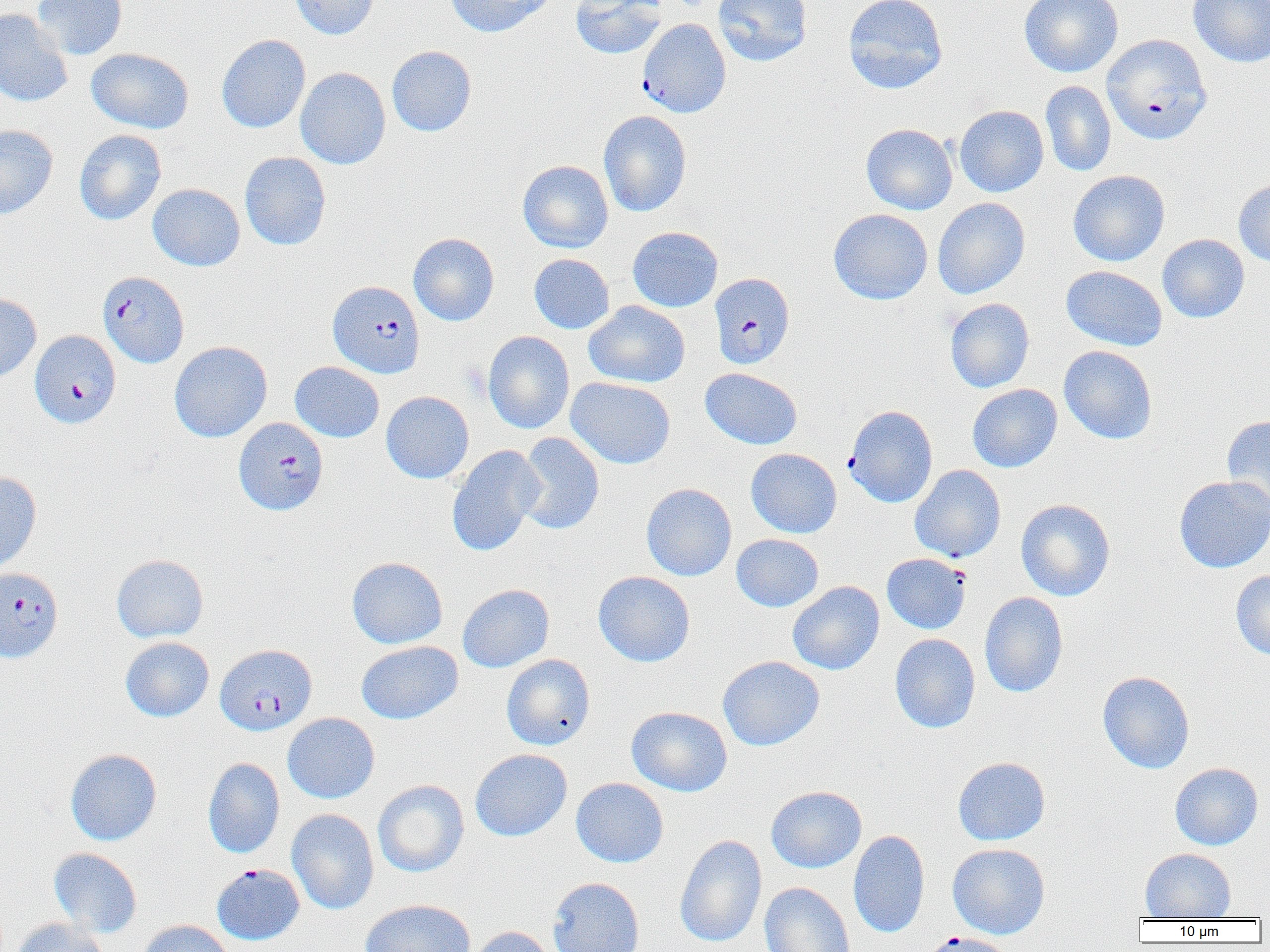
slide-level diagnosis = Plasmodium falciparum
field of view = one of a larger specimen
magnification = 1000x
uninfected red blood cell locations (subset) = approximate bounding boxes as [x1, y1, x2, y2] in pixels: [32, 0, 127, 60], [289, 0, 378, 40], [445, 0, 556, 37], [570, 0, 668, 60], [713, 0, 813, 66], [843, 0, 948, 94], [1019, 0, 1123, 78], [1187, 0, 1270, 68], [0, 9, 73, 107], [216, 34, 310, 133], [387, 45, 477, 136], [86, 48, 194, 133], [295, 67, 391, 170], [1040, 80, 1116, 177], [954, 105, 1048, 198], [598, 110, 692, 217], [860, 123, 958, 215], [0, 124, 58, 220], [74, 130, 166, 226], [239, 152, 331, 251], [517, 160, 613, 253], [1068, 170, 1170, 267], [1233, 179, 1270, 267], [148, 183, 245, 271], [932, 197, 1030, 299], [828, 208, 933, 304], [627, 226, 723, 312], [408, 233, 499, 326], [1157, 234, 1249, 323], [529, 253, 614, 334], [1060, 265, 1167, 351], [0, 293, 42, 384], [945, 298, 1034, 393], [584, 301, 689, 388], [483, 331, 574, 434], [169, 340, 272, 442], [1059, 345, 1157, 444], [289, 361, 384, 442], [700, 368, 802, 449], [566, 377, 675, 469], [967, 384, 1062, 472], [381, 391, 474, 484], [1222, 414, 1270, 514], [515, 432, 605, 535], [446, 445, 545, 557], [746, 448, 842, 538], [909, 464, 1006, 563], [0, 470, 42, 575], [1173, 475, 1270, 573], [641, 483, 737, 581], [1016, 499, 1115, 601], [731, 534, 824, 612], [111, 554, 208, 643], [346, 556, 447, 649], [881, 557, 970, 637], [1231, 570, 1270, 660], [593, 571, 695, 667], [788, 581, 885, 675], [457, 584, 554, 673], [979, 591, 1068, 697], [890, 633, 980, 733], [120, 636, 214, 722], [356, 641, 463, 724], [501, 653, 596, 750], [717, 655, 825, 751], [1097, 670, 1195, 774], [626, 706, 733, 796], [282, 712, 380, 804], [65, 748, 162, 846], [470, 748, 572, 841], [952, 756, 1050, 846], [203, 757, 285, 858], [1170, 762, 1263, 850], [571, 777, 668, 868], [373, 779, 469, 877], [766, 785, 867, 873], [287, 808, 379, 915], [848, 830, 930, 938], [674, 834, 767, 947], [947, 843, 1050, 939], [49, 848, 142, 937], [1140, 848, 1236, 920], [548, 877, 644, 952], [759, 882, 855, 952], [360, 898, 476, 952], [10, 918, 108, 952], [135, 920, 236, 952], [466, 925, 557, 952]
modality = light microscopy
Plasmodium falciparum-infected red blood cell locations (subset) = approximate bounding boxes as [x1, y1, x2, y2] in pixels: [638, 18, 731, 118], [1102, 34, 1212, 145], [98, 271, 188, 367], [709, 272, 795, 369], [328, 280, 425, 378], [29, 330, 121, 428], [233, 417, 329, 516], [0, 567, 63, 663], [215, 643, 317, 735], [211, 863, 304, 945], [919, 931, 1015, 952]
preparation = thin blood smear
image size = 1270×952 pixels